Give the extent of all Trypanosoma brucei.
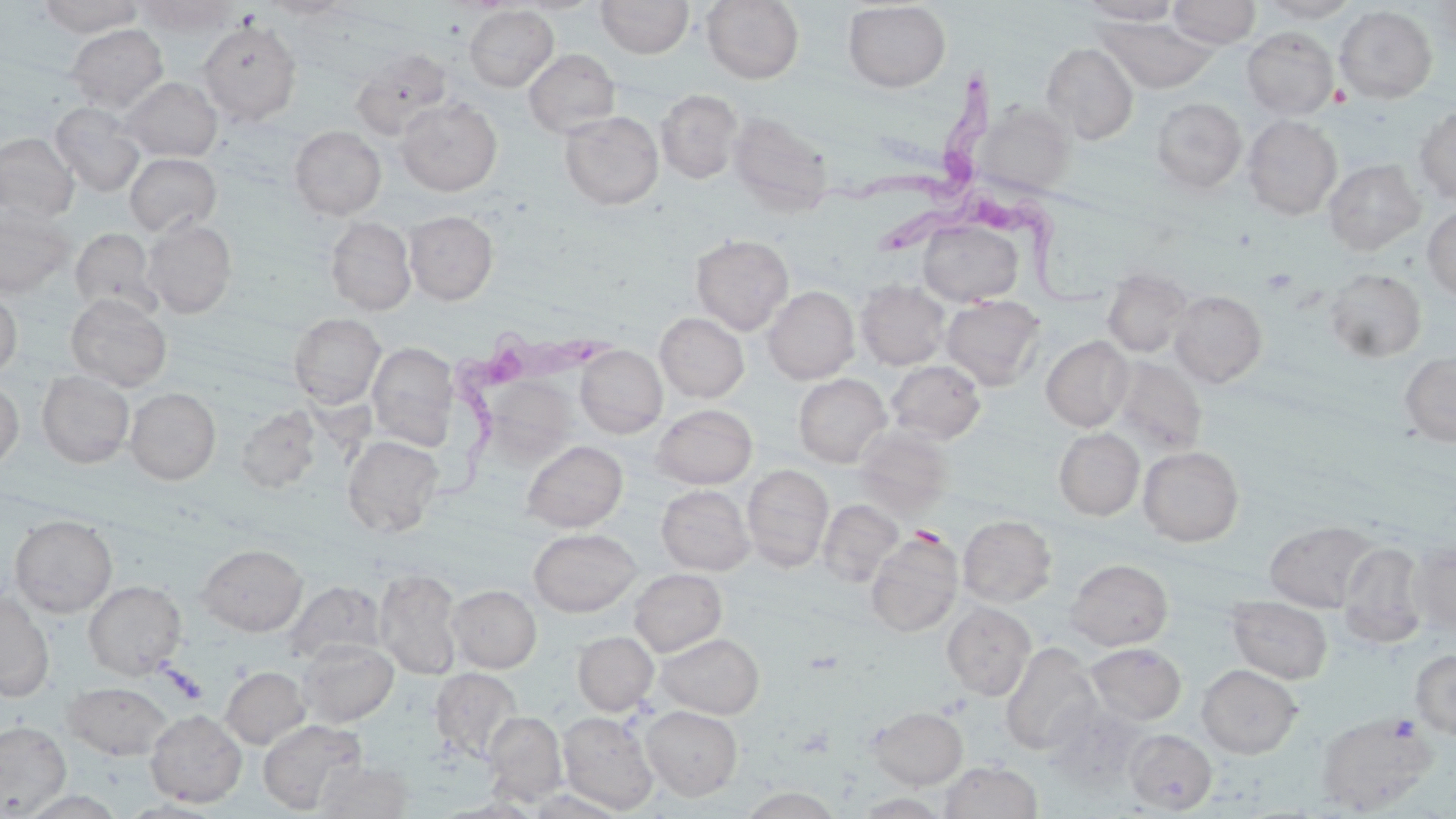

Approximate bounding boxes as (x1,y1)-(x2,y2) corner pairs in pixels.
Trypanosoma brucei: (812,72)-(1004,210), (874,199)-(1113,314), (442,324)-(618,501).

Summary:
  - Platelet locations: (1389,714)-(1420,740)
  - Uninfected red blood cell locations: (37,0)-(144,37), (261,0)-(353,19), (510,0)-(605,15), (596,0)-(694,59), (701,0)-(804,84), (1078,0)-(1184,24), (1168,0)-(1261,48), (1255,0)-(1362,23), (135,1)-(237,36), (842,2)-(951,92), (1428,2)-(1456,50), (464,5)-(558,91), (1334,5)-(1437,103), (1097,17)-(1217,93), (197,20)-(302,124), (66,24)-(168,113), (1241,27)-(1338,120), (1041,43)-(1139,144), (350,47)-(453,140), (523,48)-(620,138), (120,77)-(222,161), (655,89)-(743,184), (395,97)-(502,195), (1151,97)-(1247,193), (50,102)-(146,197), (978,104)-(1073,196), (1414,105)-(1456,206), (560,111)-(663,210), (727,111)-(833,215), (1243,115)-(1342,219), (289,125)-(386,220), (0,132)-(79,224), (124,152)-(221,236), (1324,159)-(1425,255), (0,205)-(74,297), (1422,206)-(1456,300), (404,210)-(498,304), (326,216)-(417,315), (143,218)-(236,318), (918,219)-(1024,306), (70,227)-(160,316), (690,233)-(794,335), (1103,267)-(1192,358), (1324,268)-(1426,363), (856,281)-(950,370), (763,285)-(859,383), (0,287)-(22,378), (1170,290)-(1267,387), (65,293)-(171,392), (941,294)-(1046,390), (655,312)-(749,403), (289,313)-(386,408), (1041,336)-(1133,431), (367,342)-(459,448), (575,345)-(667,438), (1399,351)-(1456,446), (1110,356)-(1206,455), (886,359)-(986,444), (37,370)-(134,468), (793,374)-(891,467), (486,378)-(574,467), (0,379)-(25,472), (125,388)-(220,485), (652,404)-(757,489), (236,405)-(322,495), (853,425)-(954,517), (1054,428)-(1144,520), (342,435)-(444,538), (522,440)-(627,532), (1138,445)-(1244,546), (742,463)-(833,572), (657,485)-(755,575), (818,499)-(903,586), (9,514)-(118,617), (958,514)-(1056,607), (1264,519)-(1379,612), (528,528)-(641,617), (866,531)-(963,637), (1408,540)-(1456,633), (1340,542)-(1428,646), (197,543)-(307,636), (1065,558)-(1173,651), (374,567)-(463,680), (629,568)-(727,656), (284,579)-(387,665), (83,580)-(187,679), (447,584)-(541,672), (0,591)-(54,701), (1227,596)-(1333,683), (942,601)-(1036,700), (573,631)-(658,715), (655,632)-(764,718), (298,639)-(398,727), (1000,642)-(1102,755), (1085,643)-(1186,725), (1410,649)-(1456,739), (1196,664)-(1303,758), (221,666)-(310,749), (431,668)-(523,763), (62,681)-(174,761), (1043,701)-(1147,793), (640,705)-(743,800), (867,706)-(968,788), (145,709)-(247,808), (483,711)-(567,805), (558,711)-(659,814), (1317,712)-(1435,814), (258,719)-(366,814), (0,720)-(71,817), (1124,729)-(1217,813), (315,760)-(413,817), (940,760)-(1043,818), (740,786)-(842,819), (526,788)-(627,818), (16,790)-(128,818), (854,793)-(951,818)
  - Slide-level diagnosis: Trypanosoma brucei
  - Field of view: single
  - Preparation: thin blood smear
  - Magnification: 1000x
  - Image size: 1456×819 pixels
  - Modality: light microscopy
  - Stain: May-Grünwald-Giemsa